Comment on the morphology of the red blood cells.
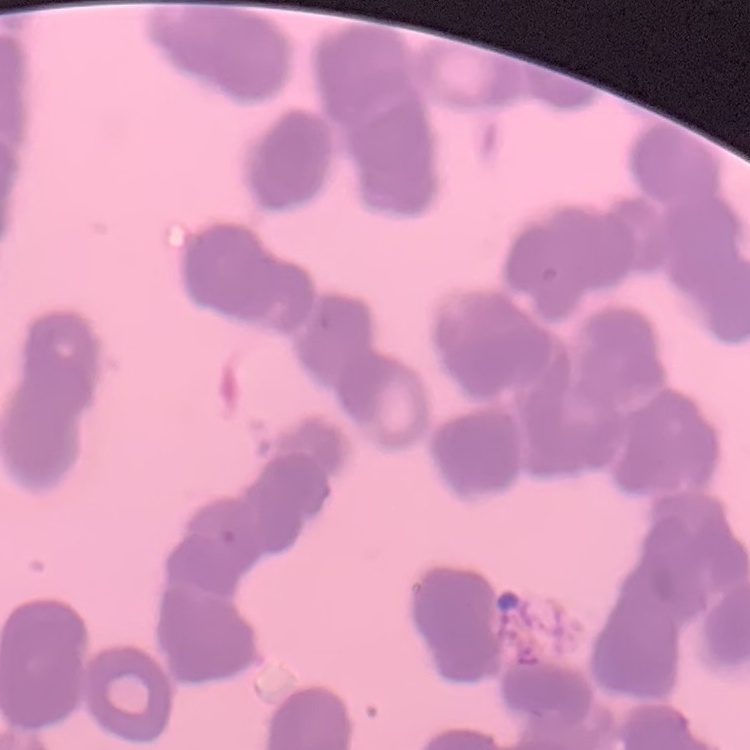

Rouleaux formation.

image_type: one tile cut from a larger photomicrograph
stain: Field's or Giemsa
preparation: thin blood film